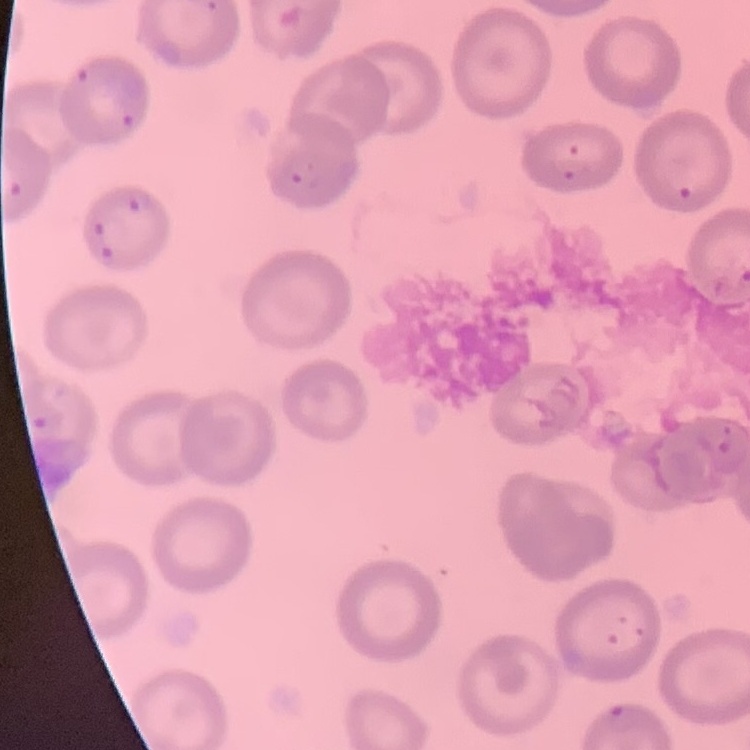

The erythrocytes show no rouleaux formation. Square crop of a larger photomicrograph. Thin blood film. Field's or Giemsa stain.